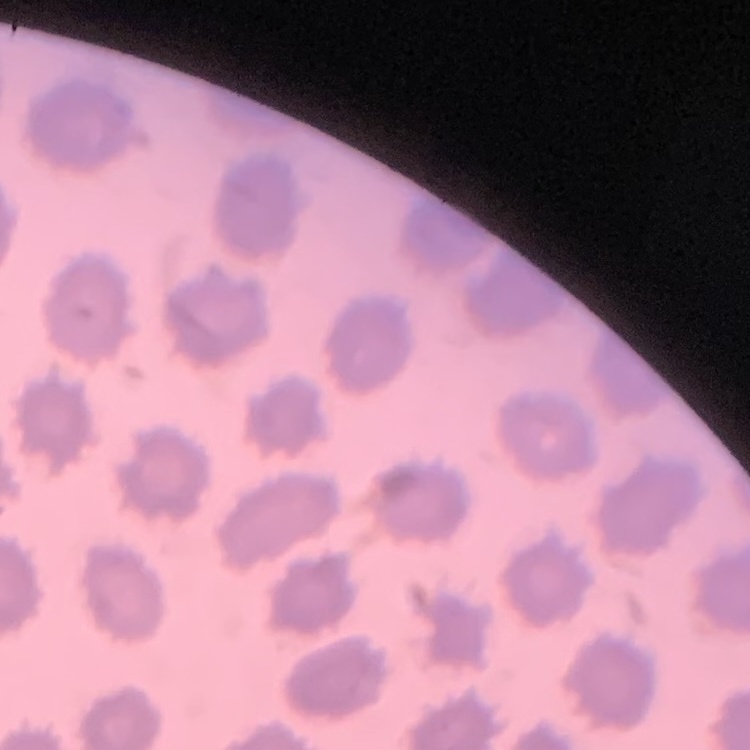 The erythrocytes show no rouleaux formation. Thin blood smear. One tile cut from a larger photomicrograph. Field's or Giemsa stain.